Describe the morphology of the erythrocytes.
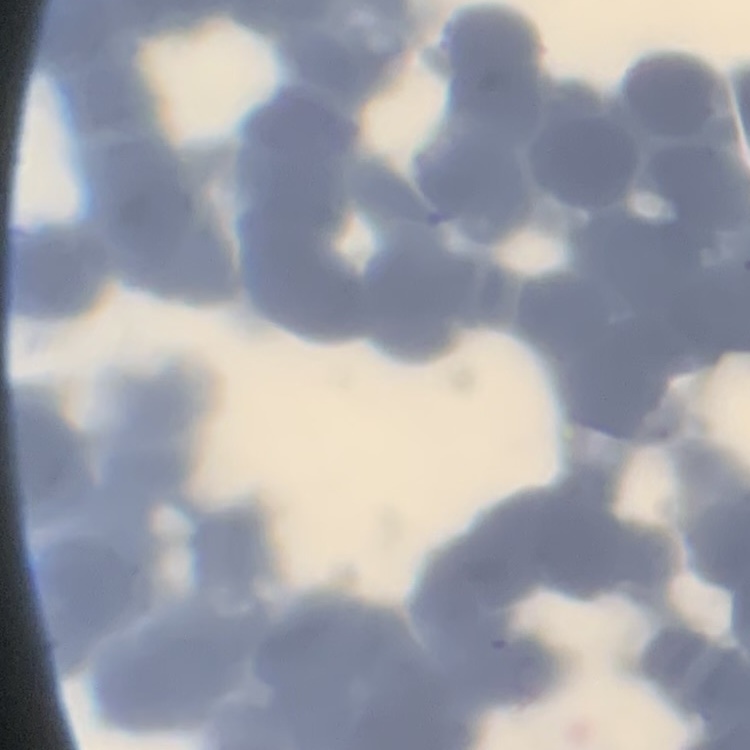
Rouleaux formation.

Summary:
  - Preparation: thin blood smear
  - Image type: square crop of a larger photomicrograph
  - Stain: Field's or Giemsa